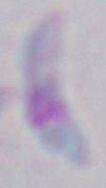
Summary:
  - Magnification: 1000x
  - Identification: Toxoplasma gondii
  - Modality: photomicrograph